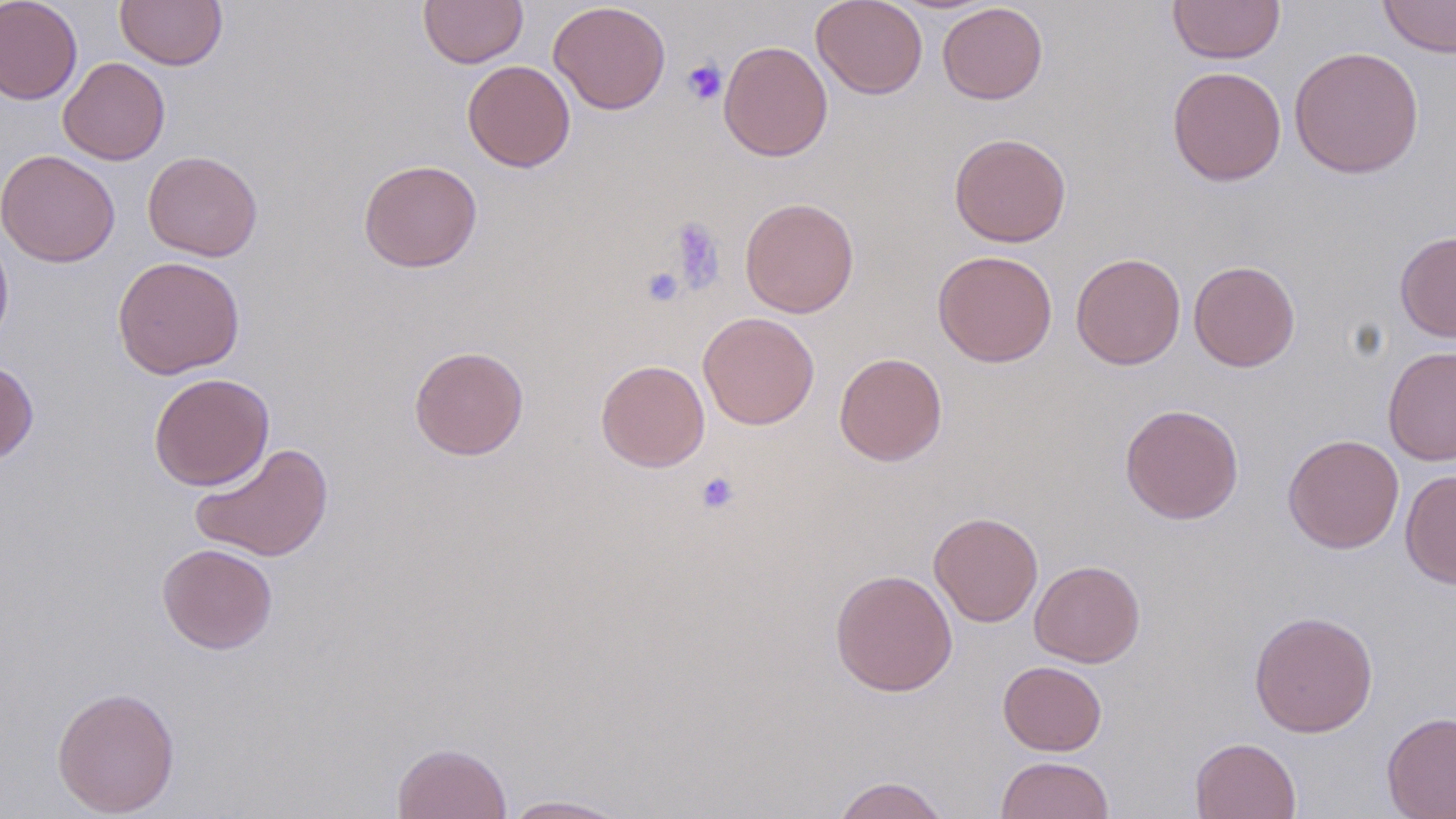

Summary:
  - Coordinate format: approximate bounding boxes as (x1,y1)-(x2,y2) corner pairs in pixels
  - Uninfected red blood cell locations: (0,0)-(83,105), (115,0)-(227,70), (418,0)-(527,68), (811,0)-(928,100), (1168,0)-(1285,64), (1378,0)-(1456,58), (548,1)-(671,115), (937,2)-(1048,104), (718,40)-(833,162), (1289,45)-(1424,179), (58,57)-(170,165), (462,60)-(575,172), (1167,66)-(1287,186), (949,132)-(1072,247), (1,149)-(120,267), (142,151)-(263,262), (358,159)-(483,272), (739,196)-(860,317), (0,226)-(14,349), (1394,230)-(1456,342), (932,250)-(1058,368), (1070,252)-(1186,369), (112,256)-(246,379), (1189,260)-(1300,372), (699,313)-(819,430), (408,345)-(529,460), (1383,345)-(1456,466), (834,352)-(948,466), (0,358)-(38,466), (596,359)-(710,472), (149,372)-(275,491), (1120,403)-(1244,524), (1282,434)-(1404,553), (190,442)-(334,562), (1400,468)-(1456,589), (929,511)-(1043,627), (157,542)-(278,654), (1029,560)-(1145,667), (830,569)-(958,696), (1249,610)-(1379,737), (998,660)-(1106,756), (52,686)-(181,817), (1381,711)-(1456,818), (1190,737)-(1301,819), (392,742)-(511,819), (995,756)-(1114,819), (832,775)-(950,819), (499,794)-(635,818)
  - Platelet locations: (681,59)-(726,105), (667,217)-(727,294), (639,266)-(685,308), (695,471)-(740,515)
  - Slide-level diagnosis: no evidence of blood parasites
  - Magnification: 1000x
  - Modality: optical microscopy
  - Preparation: thin blood smear
  - Stain: May-Grünwald-Giemsa
  - Field of view: one of a larger specimen
  - Image size: 1456×819 pixels